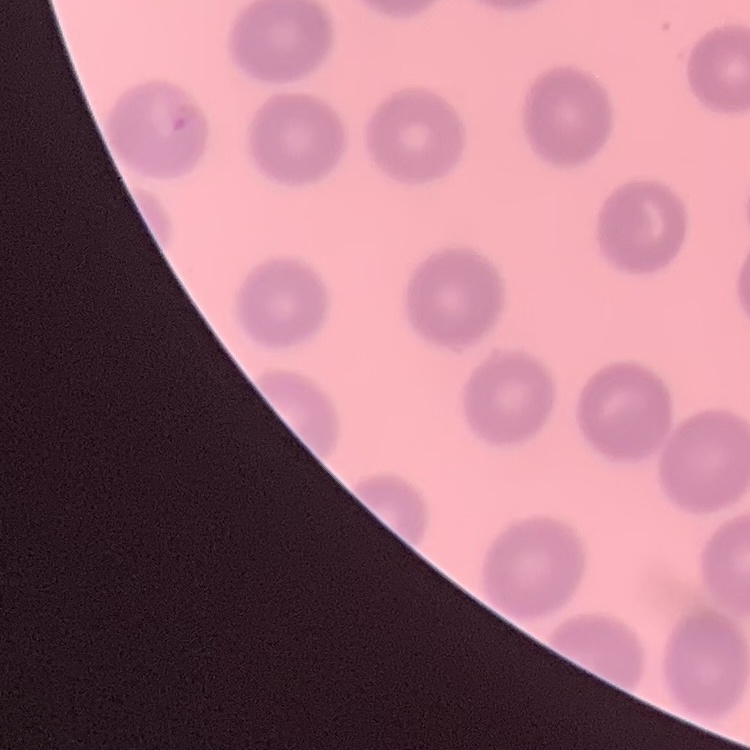

erythrocyte morphology = no rouleaux formation
stain = Field's or Giemsa
image type = one tile cut from a larger photomicrograph
preparation = thin peripheral smear